Locate every Plasmodium falciparum-infected red blood cell.
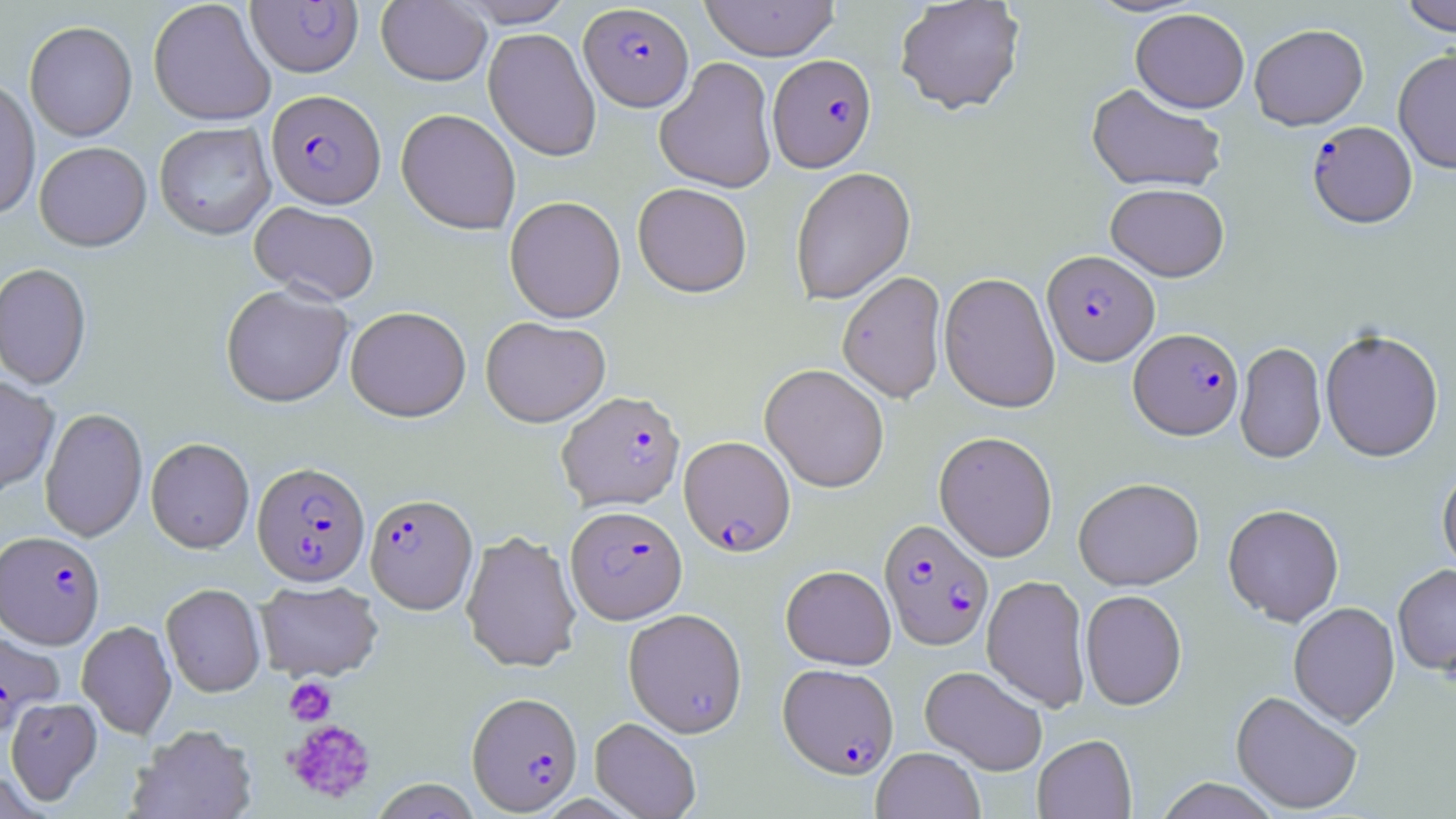

Approximate bounding boxes as [x1, y1, x2, y2] in pixels.
Plasmodium falciparum-infected red blood cells: [246, 2, 363, 77], [579, 3, 694, 111], [768, 54, 877, 173], [266, 90, 385, 209], [1307, 121, 1418, 230], [1042, 251, 1159, 367], [1129, 329, 1244, 441], [557, 390, 685, 512], [679, 436, 796, 556], [252, 461, 370, 587], [365, 493, 477, 614], [566, 505, 687, 624], [878, 519, 993, 651], [0, 531, 105, 649], [0, 629, 63, 738], [778, 663, 899, 779], [467, 692, 583, 815].

slide-level diagnosis = Plasmodium falciparum
uninfected red blood cell locations = approximate bounding boxes as [x1, y1, x2, y2] in pixels: [148, 0, 276, 126], [453, 0, 575, 27], [699, 0, 840, 61], [894, 0, 1025, 116], [1399, 0, 1456, 36], [376, 1, 491, 86], [1130, 8, 1250, 113], [24, 21, 137, 142], [1249, 24, 1368, 130], [483, 28, 601, 162], [1393, 48, 1456, 174], [655, 57, 777, 193], [0, 78, 40, 220], [1086, 84, 1227, 194], [396, 108, 521, 235], [154, 122, 276, 240], [34, 142, 152, 252], [790, 167, 916, 305], [633, 183, 752, 298], [1106, 184, 1229, 282], [504, 196, 626, 323], [250, 202, 380, 305], [0, 263, 92, 390], [837, 271, 947, 404], [938, 272, 1061, 413], [220, 284, 354, 407], [345, 306, 471, 422], [480, 316, 610, 427], [1320, 330, 1444, 463], [1235, 341, 1327, 465], [760, 364, 890, 493], [0, 376, 60, 497], [39, 408, 148, 543], [934, 431, 1058, 562], [146, 438, 254, 554], [1437, 465, 1456, 579], [1073, 478, 1204, 591], [1223, 504, 1344, 627], [460, 530, 582, 674], [1393, 564, 1456, 680], [781, 565, 896, 669], [982, 575, 1090, 712], [255, 580, 383, 683], [161, 584, 265, 697], [1080, 590, 1187, 710], [1288, 603, 1401, 729], [623, 608, 747, 737], [77, 621, 177, 739], [919, 665, 1048, 775], [1230, 691, 1362, 815], [5, 697, 103, 805], [589, 717, 701, 819], [129, 724, 258, 819], [1032, 734, 1137, 819], [871, 747, 985, 819], [1154, 778, 1281, 819], [369, 779, 483, 819]
image size = 1456×819 pixels
magnification = 1000x
modality = optical microscopy
stain = May-Grünwald-Giemsa
platelet locations = approximate bounding boxes as [x1, y1, x2, y2] in pixels: [284, 676, 337, 725], [284, 718, 377, 805]
field of view = one of a larger specimen
preparation = thin blood film